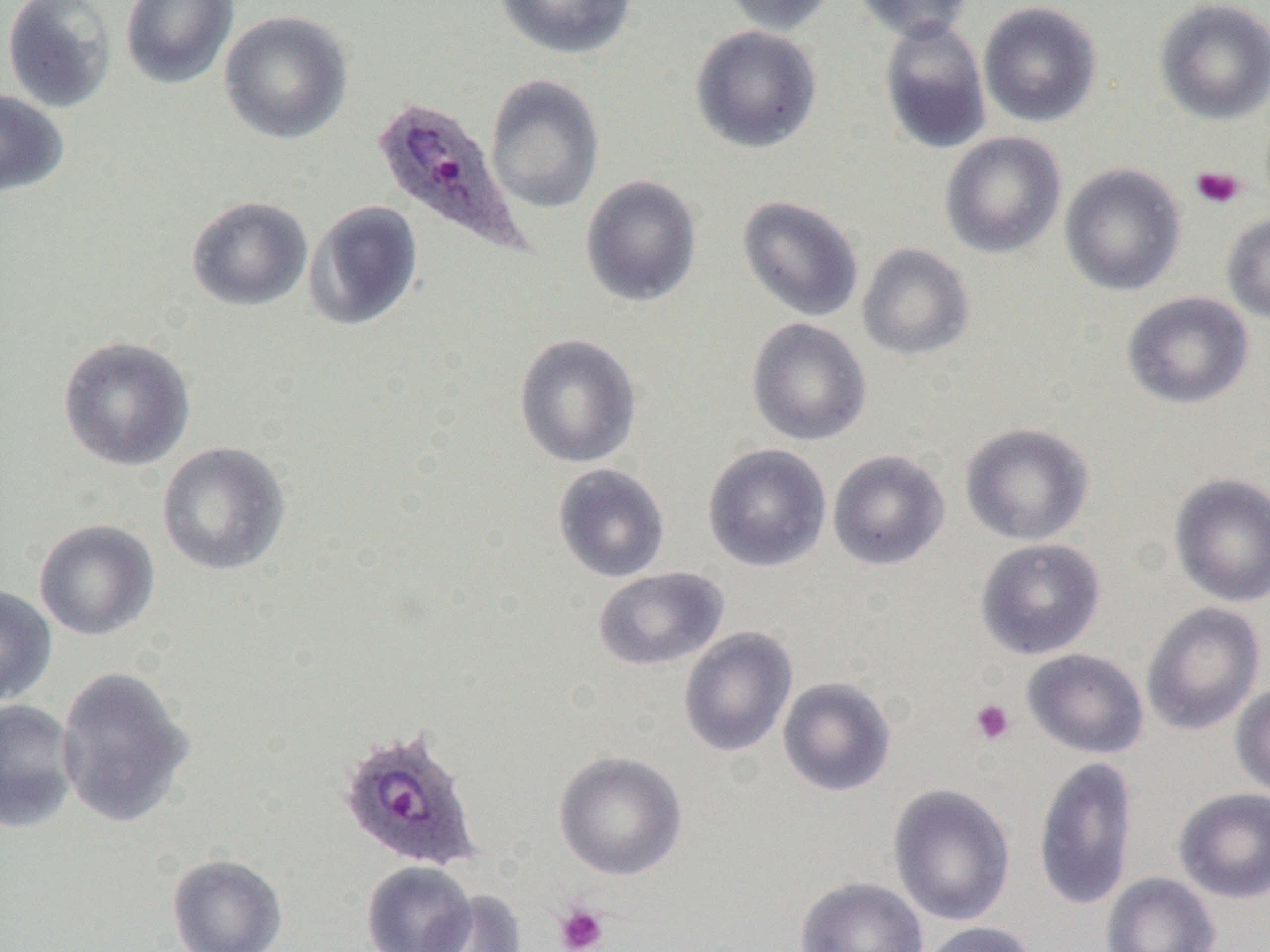

{
  "plasmodium_ovale_infected_red_blood_cell_locations": "approximate bounding boxes as (x1, y1, x2, y2) in pixels: (370, 94, 526, 255), (336, 724, 485, 873)",
  "slide_level_diagnosis": "Plasmodium ovale",
  "preparation": "thin blood film",
  "uninfected_red_blood_cell_locations": "approximate bounding boxes as (x1, y1, x2, y2) in pixels: (2, 0, 117, 114), (119, 0, 239, 90), (495, 0, 638, 60), (719, 0, 838, 35), (852, 0, 975, 43), (1154, 0, 1270, 125), (978, 1, 1102, 128), (219, 10, 353, 144), (879, 19, 992, 155), (690, 25, 822, 153), (484, 73, 605, 215), (0, 90, 69, 197), (940, 131, 1067, 258), (1060, 163, 1186, 296), (581, 175, 702, 307), (737, 195, 864, 322), (186, 196, 313, 312), (304, 200, 424, 332), (1222, 212, 1270, 323), (857, 243, 975, 361), (1121, 291, 1254, 410), (746, 318, 871, 446), (514, 334, 642, 468), (57, 335, 196, 471), (959, 422, 1094, 546), (156, 441, 292, 577), (703, 443, 831, 572), (827, 449, 950, 570), (552, 464, 670, 583), (1169, 472, 1270, 608), (33, 519, 159, 641), (975, 538, 1106, 660), (592, 566, 729, 671), (0, 585, 57, 707), (1141, 602, 1265, 736), (678, 627, 797, 757), (1022, 648, 1149, 759), (55, 665, 195, 830), (778, 677, 896, 796), (1230, 683, 1270, 798), (0, 700, 80, 833), (553, 750, 688, 880), (1032, 756, 1138, 911), (887, 783, 1016, 927), (1173, 787, 1270, 903), (166, 853, 288, 952), (361, 861, 476, 952), (1101, 872, 1220, 952), (795, 876, 928, 952), (416, 889, 527, 952), (918, 921, 1040, 952)",
  "platelet_locations": "approximate bounding boxes as (x1, y1, x2, y2) in pixels: (1190, 166, 1246, 210), (969, 698, 1016, 745), (555, 904, 608, 952)",
  "modality": "light microscopy",
  "magnification": "1000x",
  "image_size": "1270×952 pixels",
  "field_of_view": "single"
}